Evaluate for Plasmodium parasites.
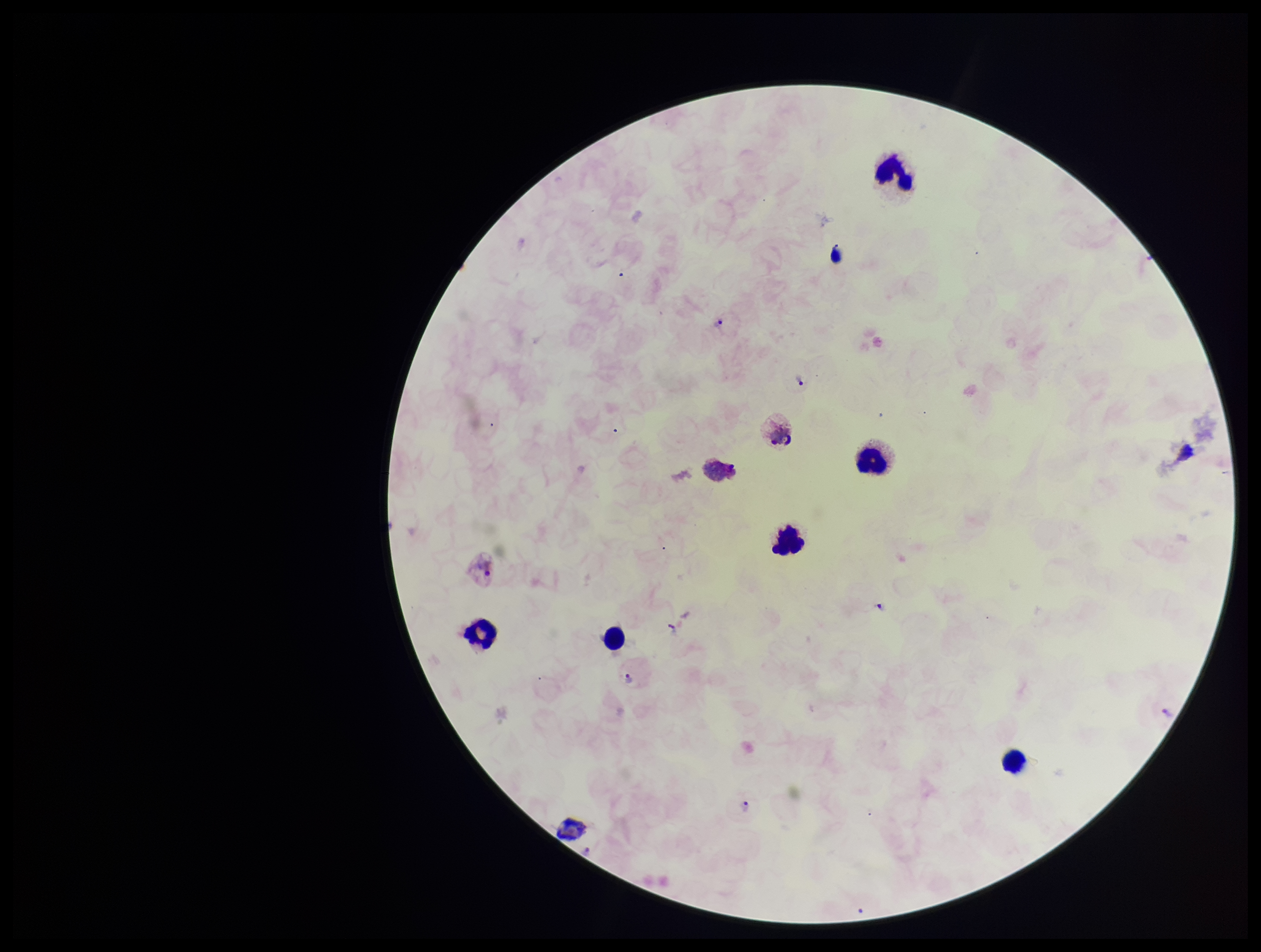

Identified.

Single field of view. Photographed through the microscope eyepiece with a smartphone camera. Parasite count: 5. Image is 1261×952 pixels. Preparation: thick smear. Stained with Giemsa. Patient malaria status: positive. Species reported for this patient: Plasmodium vivax. Leukocyte count: 7.